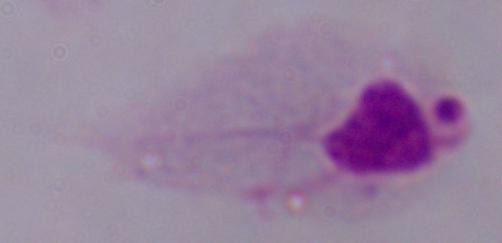
modality = micrograph
identification = trichomonad
magnification = 1000x